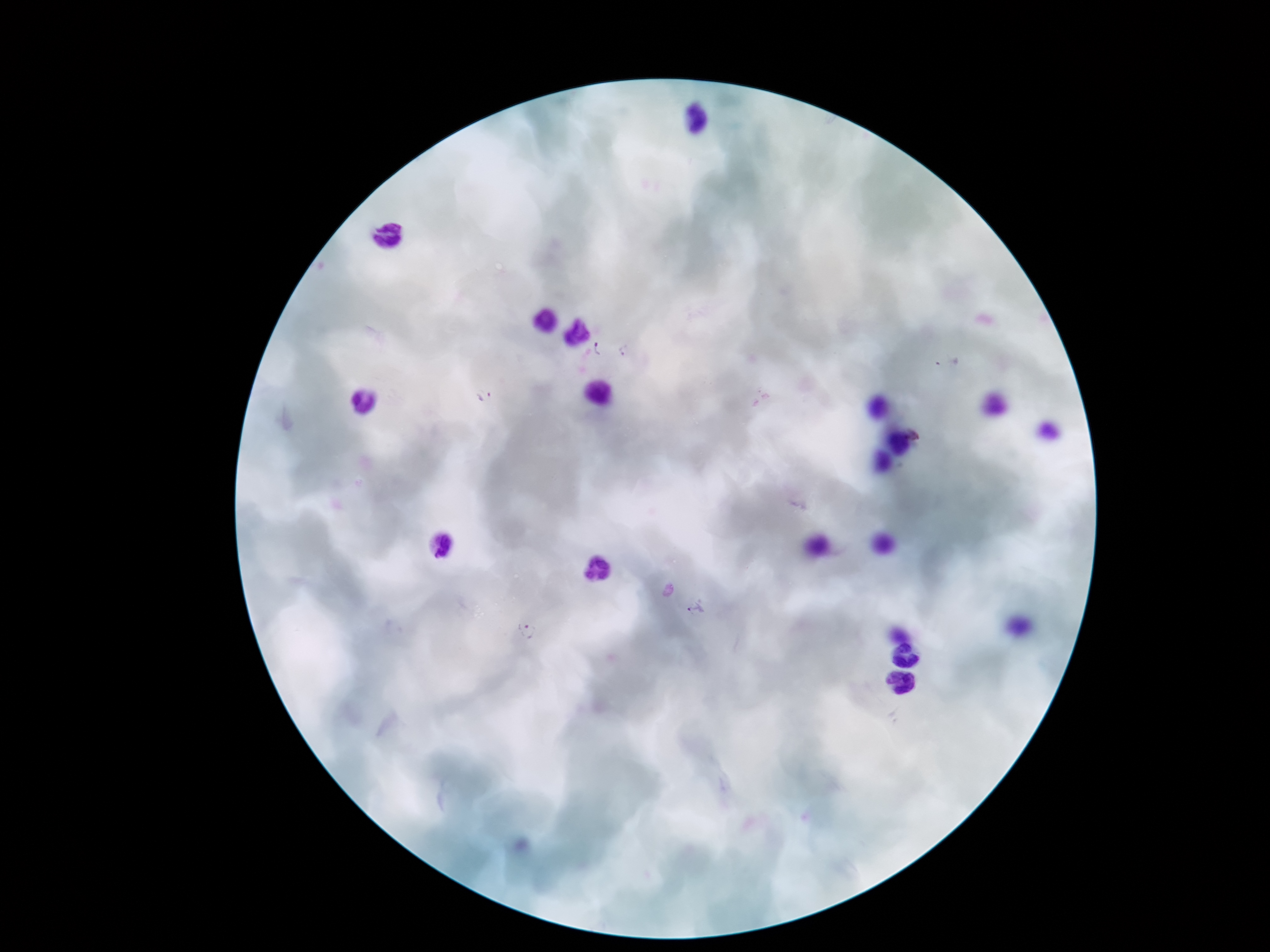 Approximate object centers, in pixels from the top-left corner. Plasmodium parasite locations: (x=601, y=348), (x=484, y=396), (x=697, y=611), (x=528, y=631). Giemsa stain. One field from this slide. Patient malaria status: positive. Smartphone photograph taken through the microscope eyepiece. 100x magnification. Thick peripheral-blood smear. Image is 1270×952 pixels.